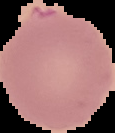
Summary:
  - Image type: cell region segmented out of the field of view; surrounding area masked to black
  - Malaria status: uninfected
  - Preparation: thin blood smear
  - Image size: 115×133 pixels